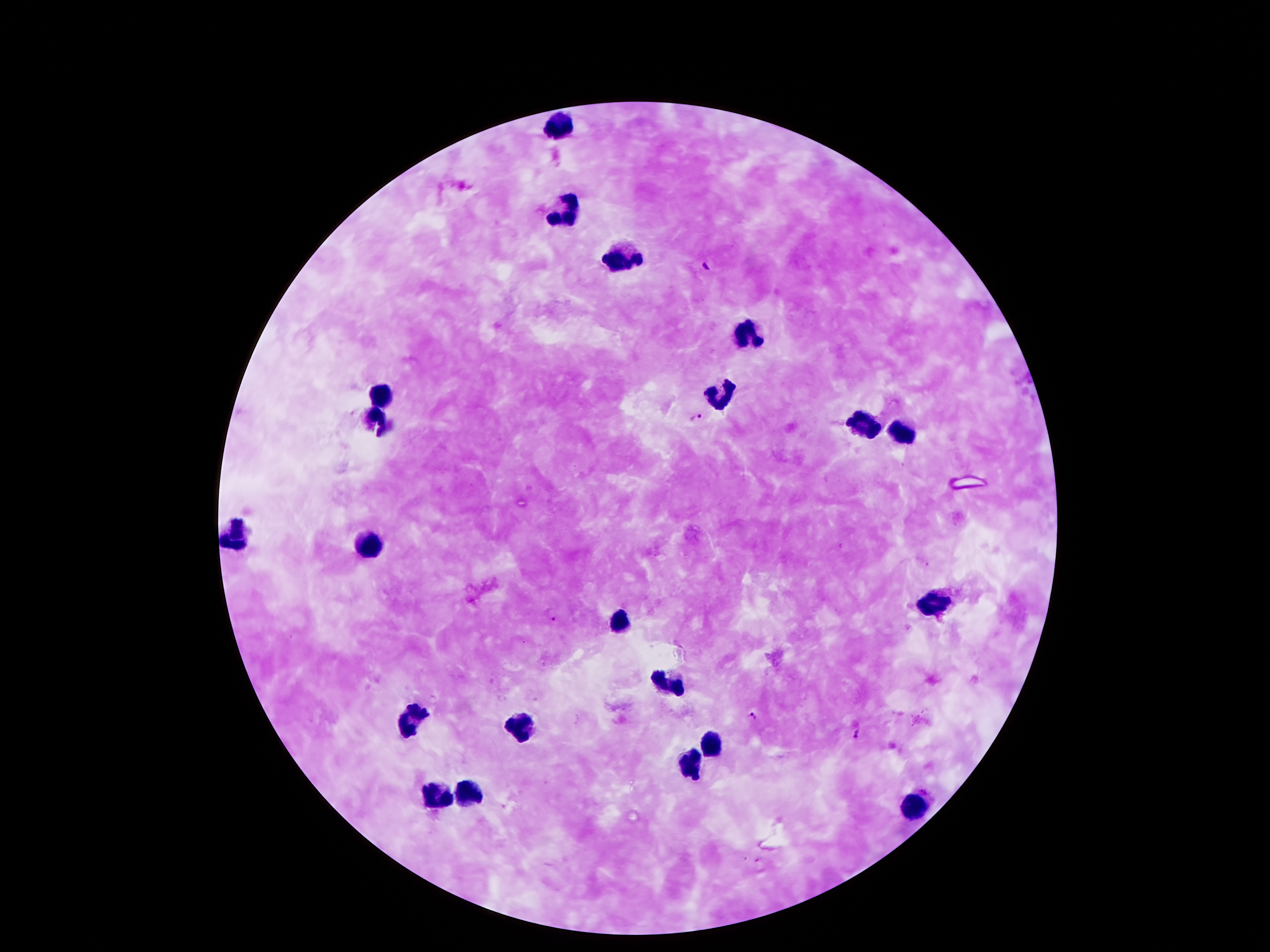
coordinate format = approximate centers as [x, y] in pixels
Plasmodium parasite locations = [706, 267], [697, 416], [552, 614], [752, 716], [856, 733]
leukocyte locations = [561, 125], [567, 211], [621, 255], [744, 329], [718, 392], [386, 394], [378, 417], [860, 422], [901, 431], [240, 530], [373, 544], [935, 598], [621, 621], [673, 683], [410, 720], [522, 733], [711, 743], [692, 763], [436, 793], [470, 793], [914, 808]
magnification = 100x
stain = Giemsa
patient malaria status = infected with Plasmodium falciparum
image size = 1270×952 pixels
field of view = single
preparation = thick blood film
capture = smartphone through the microscope eyepiece